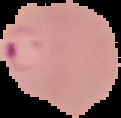
Image is 121×118 pixels. Cell region segmented out of the field of view; the surrounding area is masked to black. Malaria status: parasitized. From a thin blood smear.